State which parasite is depicted.
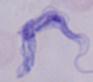

A trypanosome.

magnification = 1000x
modality = micrograph